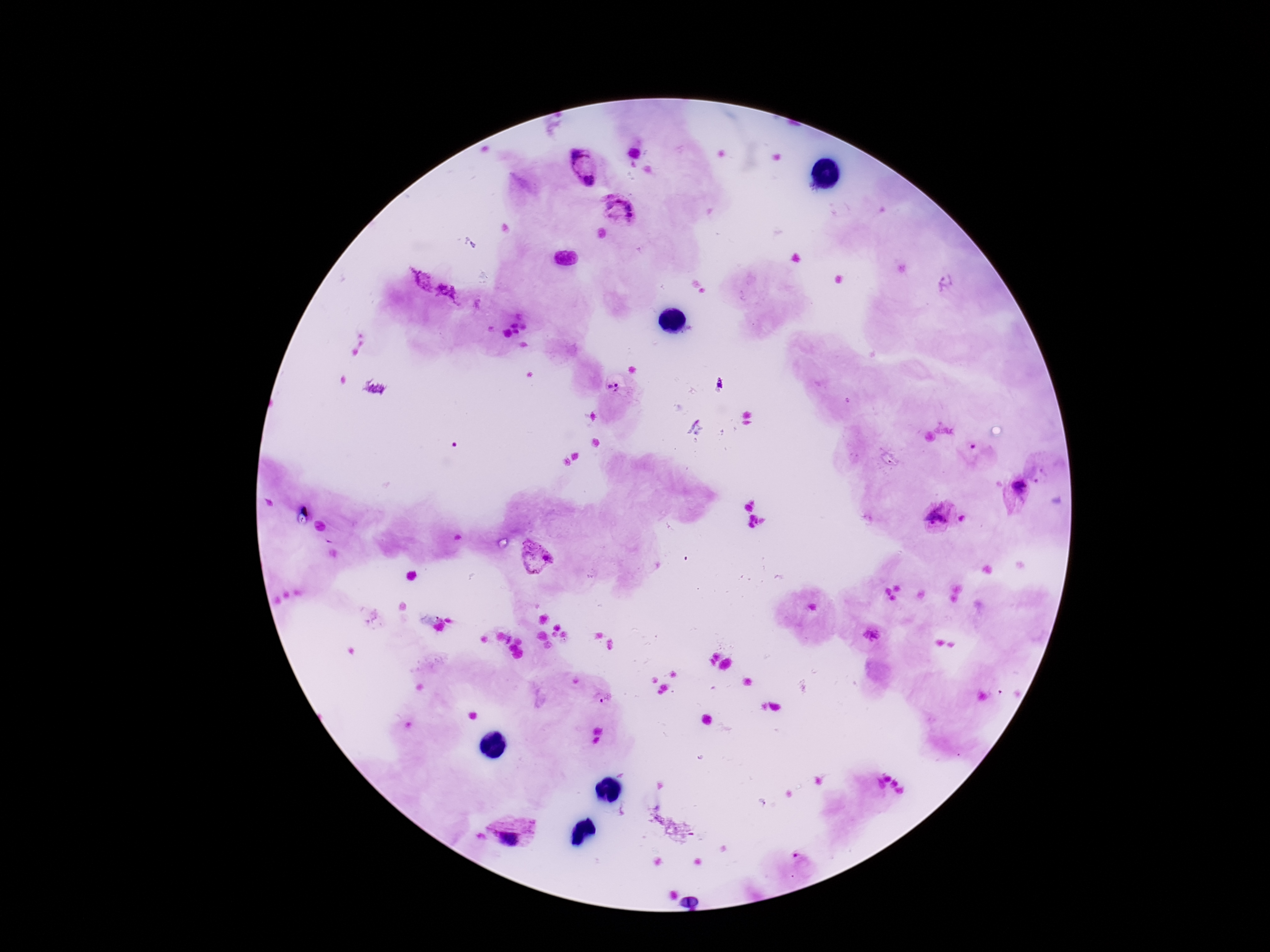
Approximate centers as {x, y} in pixels.
Summary:
  - Plasmodium parasite locations: {634, 150}, {583, 167}, {620, 209}, {947, 286}, {616, 386}, {974, 453}, {1017, 493}, {938, 518}, {537, 555}, {872, 636}, {604, 697}, {514, 830}, {799, 859}
  - Image size: 1270×952 pixels
  - Preparation: thick blood film
  - Capture: smartphone camera through the microscope eyepiece
  - Stain: Giemsa
  - Magnification: 100x
  - Field of view: single
  - Patient malaria status: positive